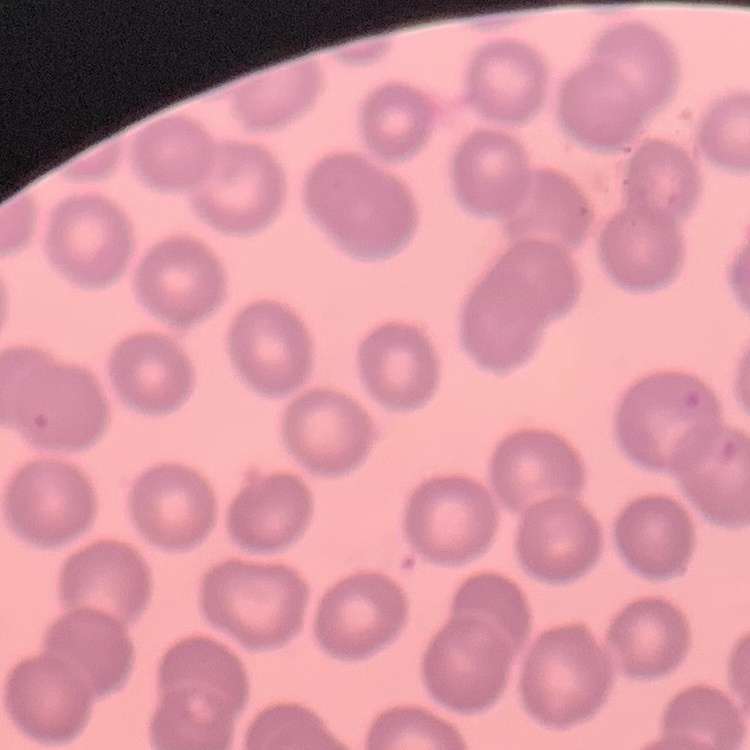
red blood cell morphology = no rouleaux formation
preparation = thin blood film
image type = square crop of a larger photomicrograph
stain = Field's or Giemsa